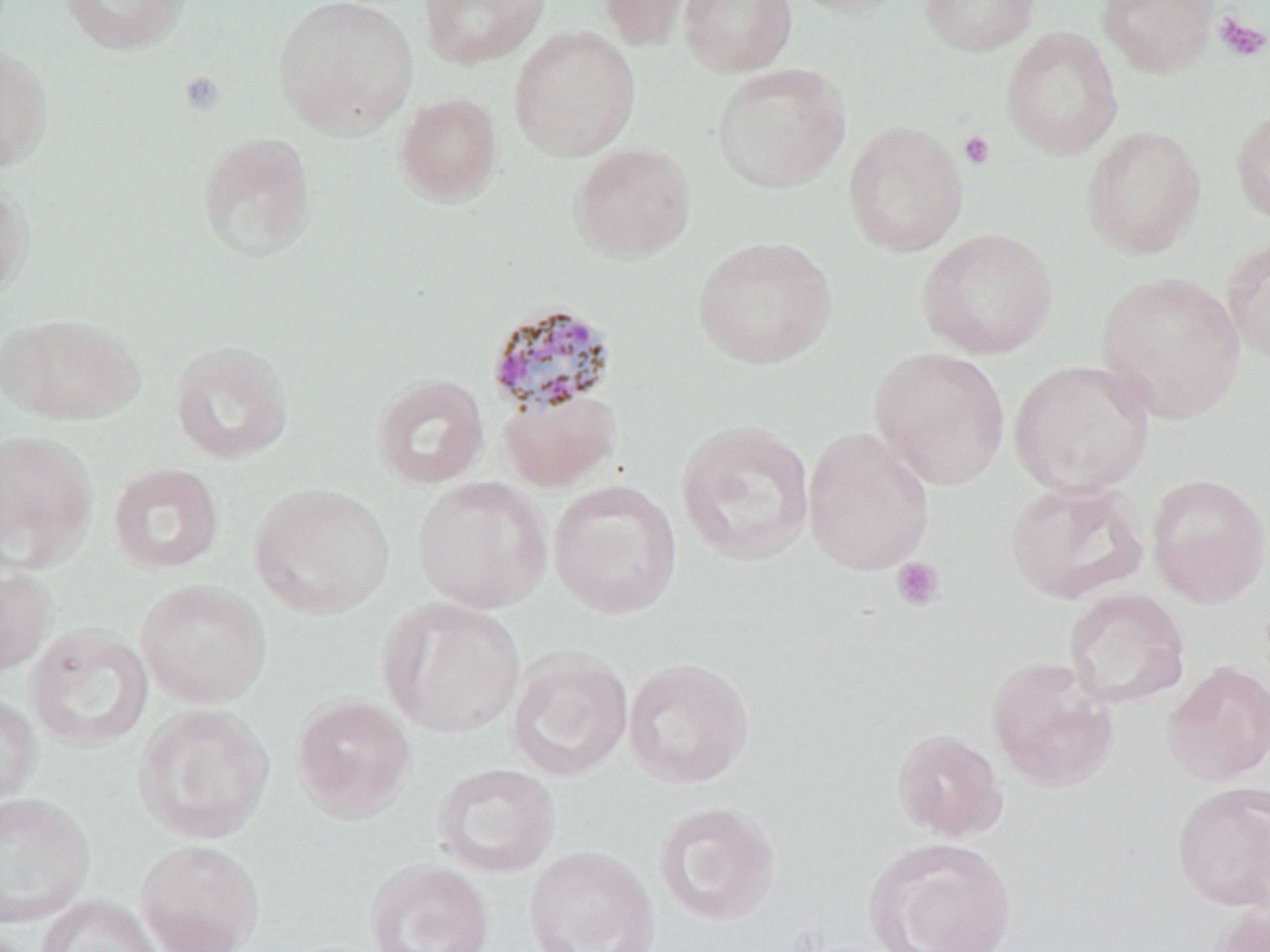
Summary:
  - Coordinate format: approximate bounding boxes as (x1,y1)-(x2,y2) corner pairs in pixels
  - Platelet locations: (1213,13)-(1270,62), (178,70)-(225,116), (958,130)-(996,170), (890,556)-(946,612)
  - Plasmodium malariae-infected red blood cell locations: (485,301)-(618,416)
  - Uninfected red blood cell locations: (59,0)-(193,55), (272,0)-(419,140), (418,0)-(549,68), (600,0)-(694,52), (678,0)-(797,76), (785,0)-(914,18), (919,0)-(1040,56), (1097,0)-(1220,77), (508,25)-(641,161), (1000,26)-(1123,160), (0,44)-(53,173), (712,62)-(851,193), (394,92)-(503,206), (1230,103)-(1270,226), (843,119)-(969,258), (1081,125)-(1208,259), (196,132)-(316,263), (569,142)-(697,263), (0,176)-(34,304), (916,228)-(1059,360), (1222,235)-(1270,366), (693,236)-(838,369), (1096,271)-(1247,423), (1,313)-(144,426), (168,339)-(294,464), (869,346)-(1011,490), (1009,359)-(1156,496), (371,372)-(489,490), (498,389)-(621,492), (675,419)-(817,567), (803,425)-(935,576), (0,429)-(97,572), (107,463)-(224,575), (1147,473)-(1270,608), (412,475)-(552,613), (1004,477)-(1150,604), (547,479)-(683,619), (249,482)-(395,619), (0,560)-(55,678), (135,579)-(271,708), (1062,587)-(1191,710), (378,597)-(526,738), (25,623)-(154,751), (506,648)-(634,782), (985,655)-(1119,792), (622,657)-(755,789), (1161,660)-(1270,786), (0,693)-(40,813), (290,694)-(417,823), (131,702)-(275,845), (891,727)-(1007,841), (433,763)-(560,879), (1171,782)-(1270,911), (0,792)-(94,929), (653,800)-(782,928), (866,837)-(1017,952), (136,839)-(264,952), (523,846)-(661,952), (364,858)-(495,952), (34,895)-(165,952), (1205,899)-(1270,952)
  - Slide-level diagnosis: Plasmodium malariae
  - Magnification: 1000x
  - Preparation: thin blood film
  - Image size: 1270×952 pixels
  - Modality: optical microscopy
  - Field of view: single
  - Stain: May-Grünwald-Giemsa